Classify this cell by malaria status.
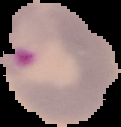

Parasitized.

image size = 121×127 pixels
image type = cell region segmented out of the field of view; surrounding area masked to black
preparation = thin blood film